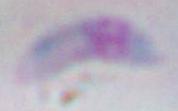

Summary:
  - Modality: photomicrograph
  - Identification: Toxoplasma gondii
  - Magnification: 1000x